Outline each blood parasite and name the species.
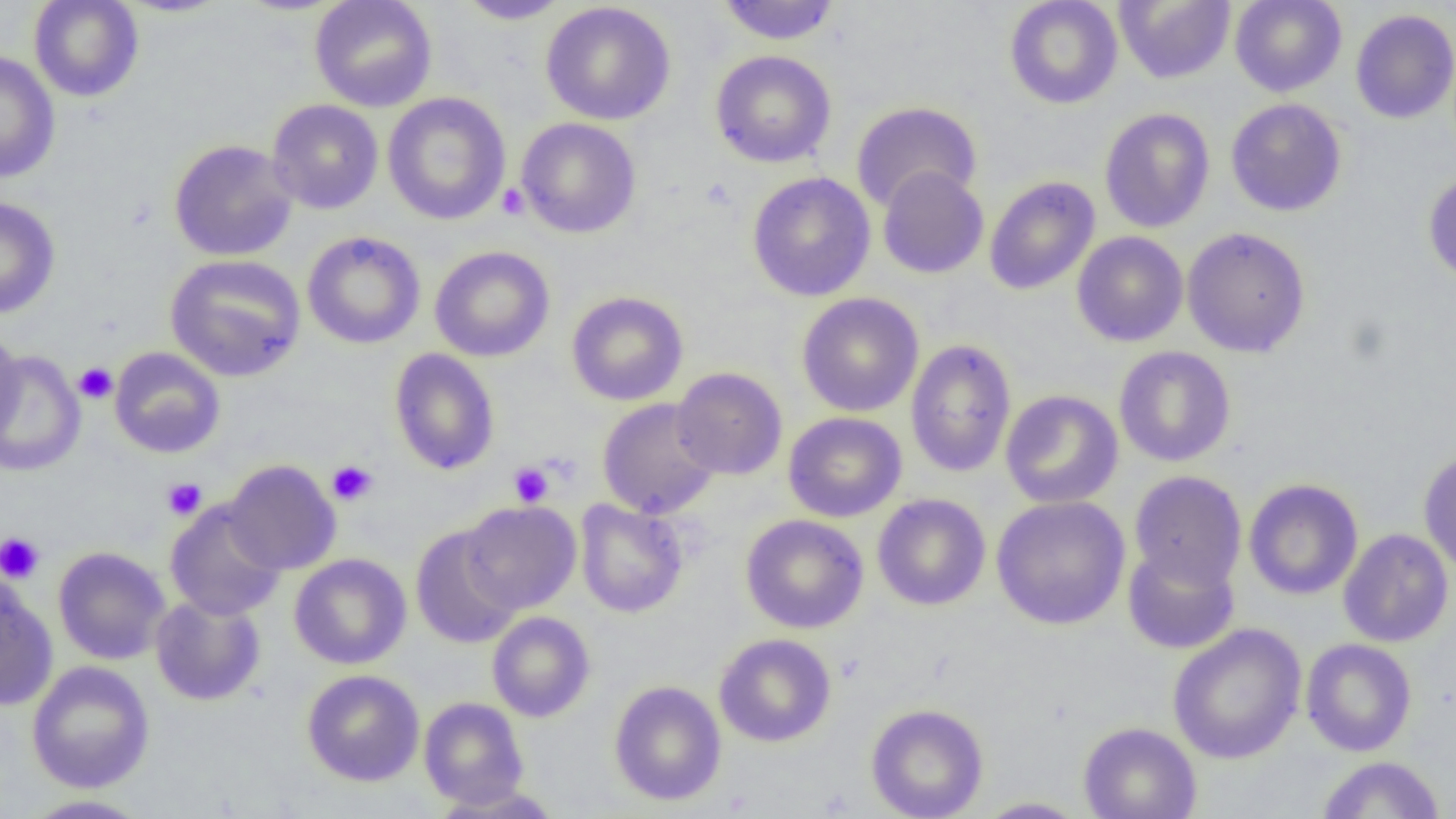
No blood parasites seen.

Approximate bounding boxes as [x1, y1, x2, y2] in pixels. Platelet locations: [497, 183, 530, 219], [73, 362, 117, 403], [327, 460, 378, 506], [509, 462, 553, 507], [161, 477, 207, 520], [0, 531, 45, 584]. Uninfected red blood cell locations: [29, 0, 144, 102], [309, 0, 437, 112], [454, 0, 572, 25], [1004, 0, 1123, 109], [1114, 0, 1236, 84], [1230, 0, 1347, 97], [541, 1, 676, 125], [717, 1, 841, 45], [1350, 9, 1456, 124], [1, 50, 61, 183], [710, 50, 837, 168], [382, 92, 511, 225], [1225, 98, 1347, 217], [267, 99, 384, 215], [851, 101, 982, 213], [1091, 107, 1199, 347], [1099, 107, 1216, 233], [516, 117, 641, 238], [168, 139, 299, 261], [877, 166, 989, 279], [1422, 171, 1456, 286], [747, 172, 876, 301], [984, 176, 1100, 295], [0, 197, 61, 318], [1182, 227, 1311, 358], [302, 231, 426, 349], [1072, 231, 1188, 347], [429, 245, 555, 362], [165, 254, 306, 381], [567, 290, 688, 406], [796, 292, 924, 417], [0, 328, 24, 446], [905, 338, 1017, 478], [1114, 346, 1236, 467], [110, 347, 226, 458], [389, 348, 501, 475], [1, 351, 85, 476], [671, 367, 788, 480], [1000, 390, 1123, 508], [597, 397, 721, 520], [783, 412, 907, 522], [1418, 449, 1456, 575], [224, 460, 341, 575], [1129, 471, 1247, 590], [1243, 478, 1363, 600], [872, 493, 990, 611], [991, 495, 1131, 630], [164, 499, 287, 621], [574, 499, 688, 618], [460, 501, 581, 613], [740, 514, 868, 634], [411, 526, 522, 648], [1338, 528, 1454, 648], [1122, 543, 1240, 654], [52, 546, 170, 665], [289, 554, 411, 669], [0, 575, 58, 711], [150, 594, 265, 706], [487, 612, 595, 722], [1167, 623, 1307, 764], [714, 633, 837, 747], [1301, 639, 1417, 756], [27, 660, 155, 793], [302, 669, 425, 786], [609, 680, 726, 806], [419, 696, 529, 809], [865, 703, 989, 819], [1078, 721, 1201, 819], [1317, 755, 1445, 818], [428, 783, 565, 818], [19, 794, 154, 818], [973, 797, 1088, 818]. Slide-level diagnosis: negative for blood parasites. One field of a larger specimen. Image is 1456×819 pixels. Light microscopy. Captured at 1000x magnification. Thin blood smear.